Assess the morphology of the erythrocytes.
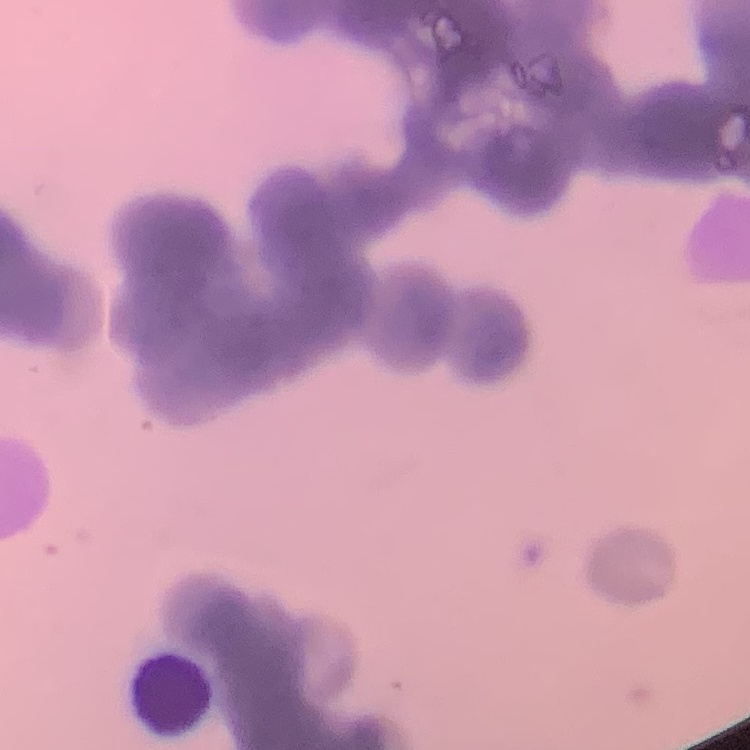

They show rouleaux formation.

Square crop of a larger photomicrograph. Field's or Giemsa stain. Thin peripheral smear.